Identify the blood parasite species.
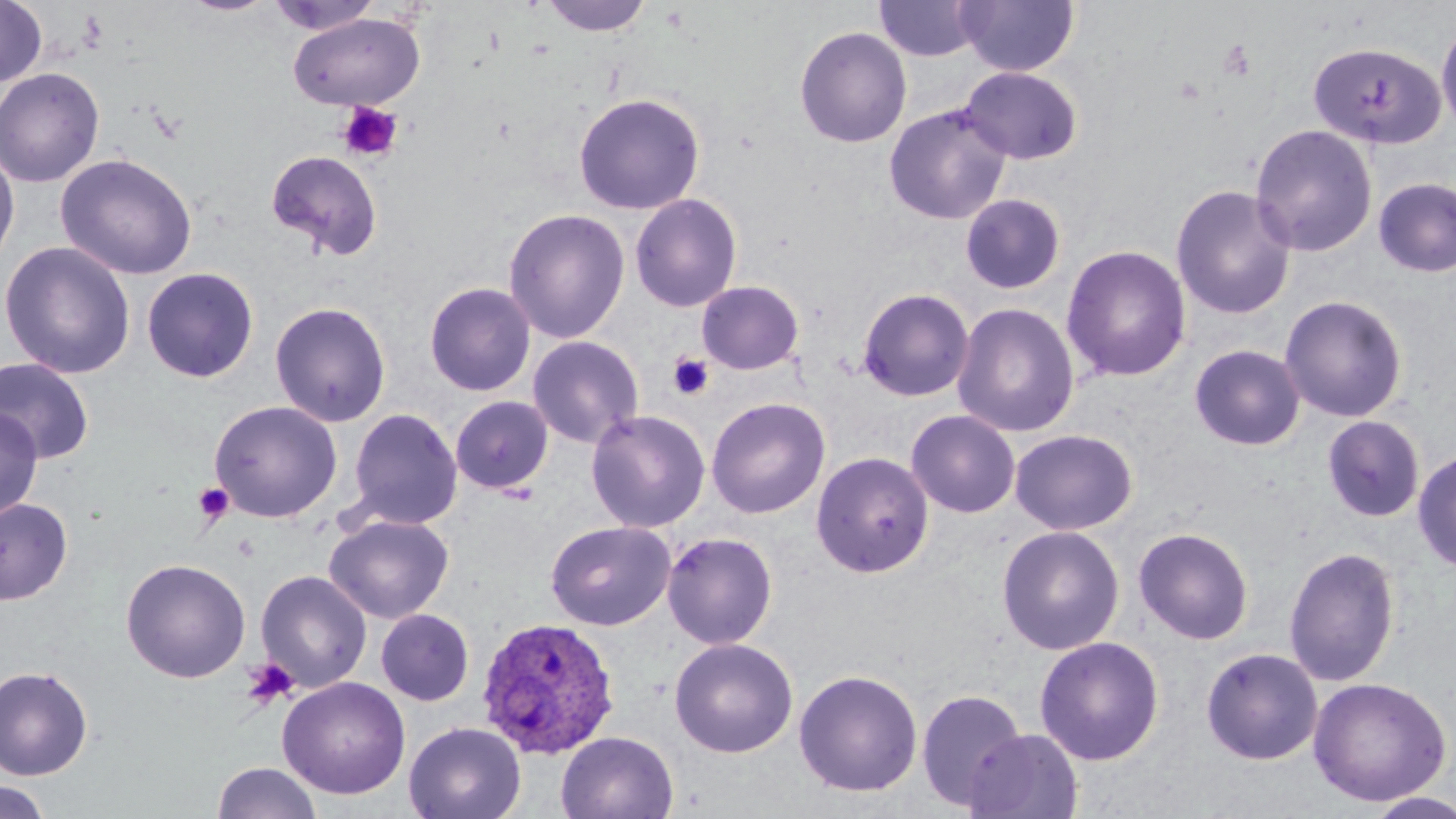

Plasmodium ovale.

magnification: 1000x
stain: May-Grünwald-Giemsa
platelet_locations: 'approximate bounding boxes as [x1, y1, x2, y2] in pixels: [1218, 40, 1256, 81], [337, 101, 403, 162], [667, 352, 714, 401], [193, 482, 235, 526], [233, 535, 260, 562], [241, 658, 300, 710]'
image_size: 1456×819 pixels
field_of_view: single
plasmodium_ovale_infected_red_blood_cell_locations: 'approximate bounding boxes as [x1, y1, x2, y2] in pixels: [476, 616, 619, 759]'
preparation: thin blood smear
uninfected_red_blood_cell_locations: 'approximate bounding boxes as [x1, y1, x2, y2] in pixels: [180, 0, 277, 16], [539, 0, 655, 37], [875, 0, 982, 61], [955, 0, 1079, 76], [0, 1, 47, 88], [265, 1, 382, 36], [288, 13, 425, 111], [1436, 16, 1456, 139], [794, 26, 912, 148], [1307, 40, 1445, 150], [960, 66, 1083, 164], [0, 67, 105, 188], [573, 92, 705, 214], [883, 103, 1013, 225], [1249, 123, 1378, 257], [0, 144, 20, 274], [265, 149, 384, 260], [55, 152, 198, 280], [1373, 177, 1456, 278], [1170, 184, 1297, 321], [629, 193, 743, 313], [960, 193, 1065, 294], [503, 208, 630, 344], [0, 241, 136, 380], [1061, 244, 1192, 382], [141, 267, 259, 383], [424, 281, 536, 396], [696, 281, 804, 375], [857, 287, 975, 402], [1279, 295, 1408, 422], [270, 301, 391, 427], [952, 303, 1080, 437], [526, 335, 645, 449], [1190, 344, 1306, 451], [0, 357, 95, 464], [450, 396, 553, 494], [706, 397, 830, 519], [208, 400, 343, 523], [0, 406, 43, 521], [347, 407, 463, 529], [906, 409, 1020, 518], [585, 410, 711, 533], [1322, 415, 1425, 522], [1009, 429, 1138, 535], [1412, 448, 1456, 573], [811, 451, 934, 578], [0, 497, 73, 605], [325, 513, 454, 624], [545, 520, 675, 631], [996, 524, 1125, 655], [1133, 527, 1254, 645], [662, 531, 778, 649], [1283, 546, 1401, 686], [120, 558, 251, 683], [255, 570, 373, 692], [376, 609, 475, 706], [1034, 635, 1165, 766], [669, 637, 798, 758], [1200, 646, 1323, 765], [0, 665, 93, 779], [793, 669, 923, 797], [276, 676, 411, 799], [1308, 676, 1451, 805], [916, 687, 1027, 810], [404, 721, 526, 819], [965, 728, 1084, 819], [556, 730, 678, 819], [212, 761, 323, 819], [1, 780, 54, 818], [1363, 792, 1456, 818]'
modality: optical microscopy